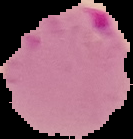

Image is 133×139 pixels. The area outside the segmented cell region is set to black. Malaria status: parasitized. From a thin blood film.